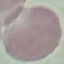 Result: no malaria parasites seen. Photographed with a smartphone camera at the microscope eyepiece. Cell patch, automatically extracted from a larger field of view and resized to 64 × 64 pixels. Thin smear of blood. Giemsa stain.